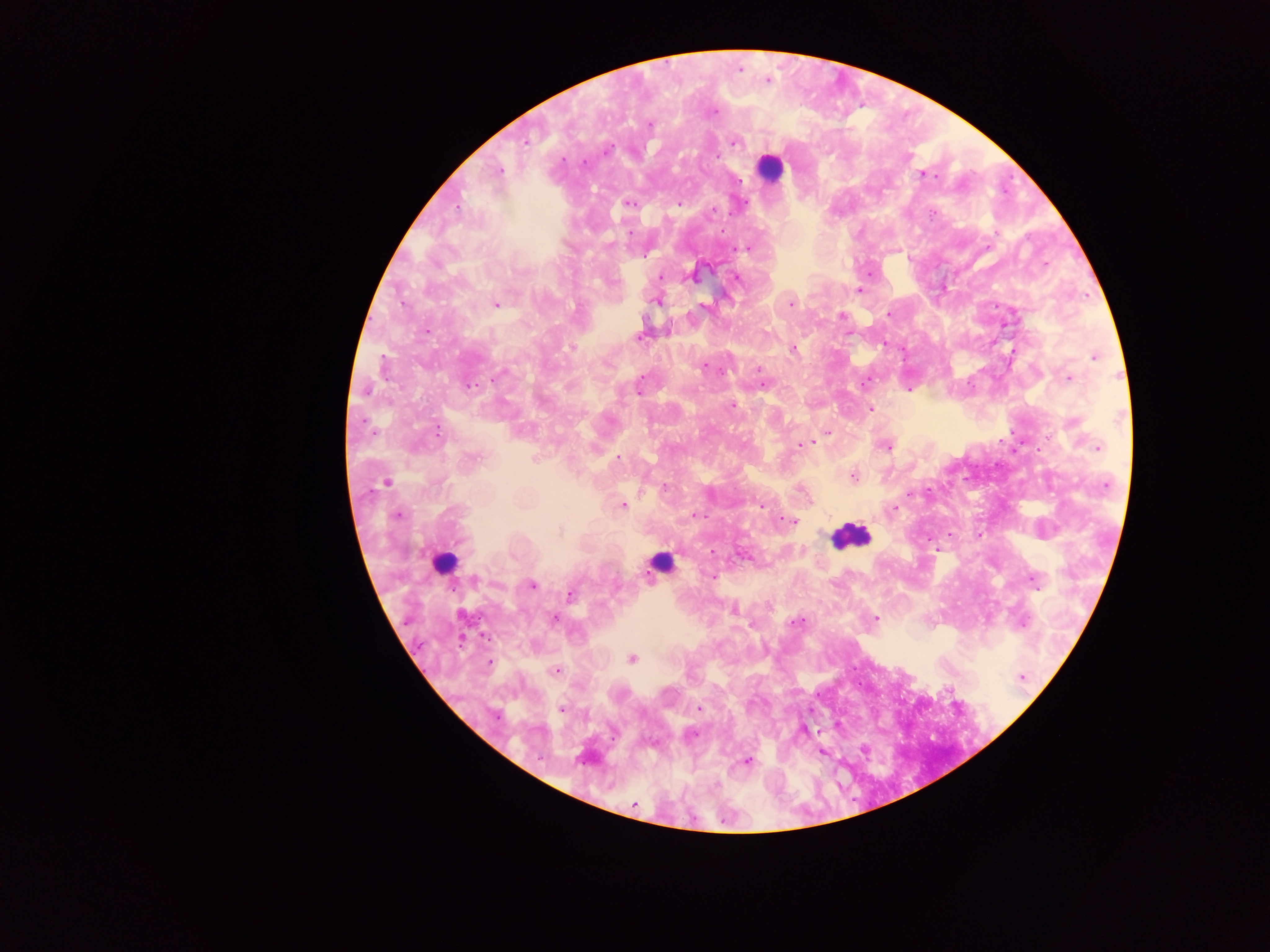

Approximate centers as [x, y] in pixels.
Summary:
  - Leukocyte locations: [772, 166], [850, 535], [442, 562], [660, 562]
  - Malaria parasite locations: [740, 69], [767, 81], [715, 112], [649, 124], [526, 142], [734, 142], [607, 150], [563, 160], [585, 162], [498, 172], [926, 174], [740, 181], [628, 203], [744, 203], [679, 204], [458, 207], [712, 210], [934, 214], [629, 232], [609, 244], [747, 248], [646, 255], [1046, 263], [660, 277], [692, 277], [737, 278], [859, 291], [656, 301], [403, 303], [791, 303], [495, 304], [704, 306], [888, 314], [842, 315], [426, 330], [640, 337], [884, 344], [571, 347], [793, 349], [1095, 357], [705, 365], [759, 369], [498, 376], [1069, 379], [640, 380], [864, 382], [763, 384], [469, 385], [366, 390], [639, 390], [732, 406], [871, 409], [438, 431], [828, 433], [810, 442], [803, 445], [886, 446], [1097, 447], [474, 458], [618, 458], [534, 459], [853, 476], [385, 482], [1105, 485], [665, 487], [623, 506], [760, 506], [894, 508], [397, 515], [697, 516], [792, 522], [712, 551], [744, 556], [712, 576], [476, 580], [1033, 581], [533, 585], [570, 595], [734, 610], [875, 618], [555, 620], [795, 622], [1022, 623], [632, 659], [490, 663], [556, 671], [1021, 676], [699, 709], [562, 710], [497, 716], [804, 730], [692, 734], [746, 761], [633, 804]
  - Country: Ghana
  - Field of view: single
  - Capture: mobile-phone photograph through a microscope
  - Preparation: thick blood smear
  - Image size: 1270×952 pixels